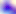
Captured at 400x magnification. Toxoplasma gondii is shown. Photomicrograph.